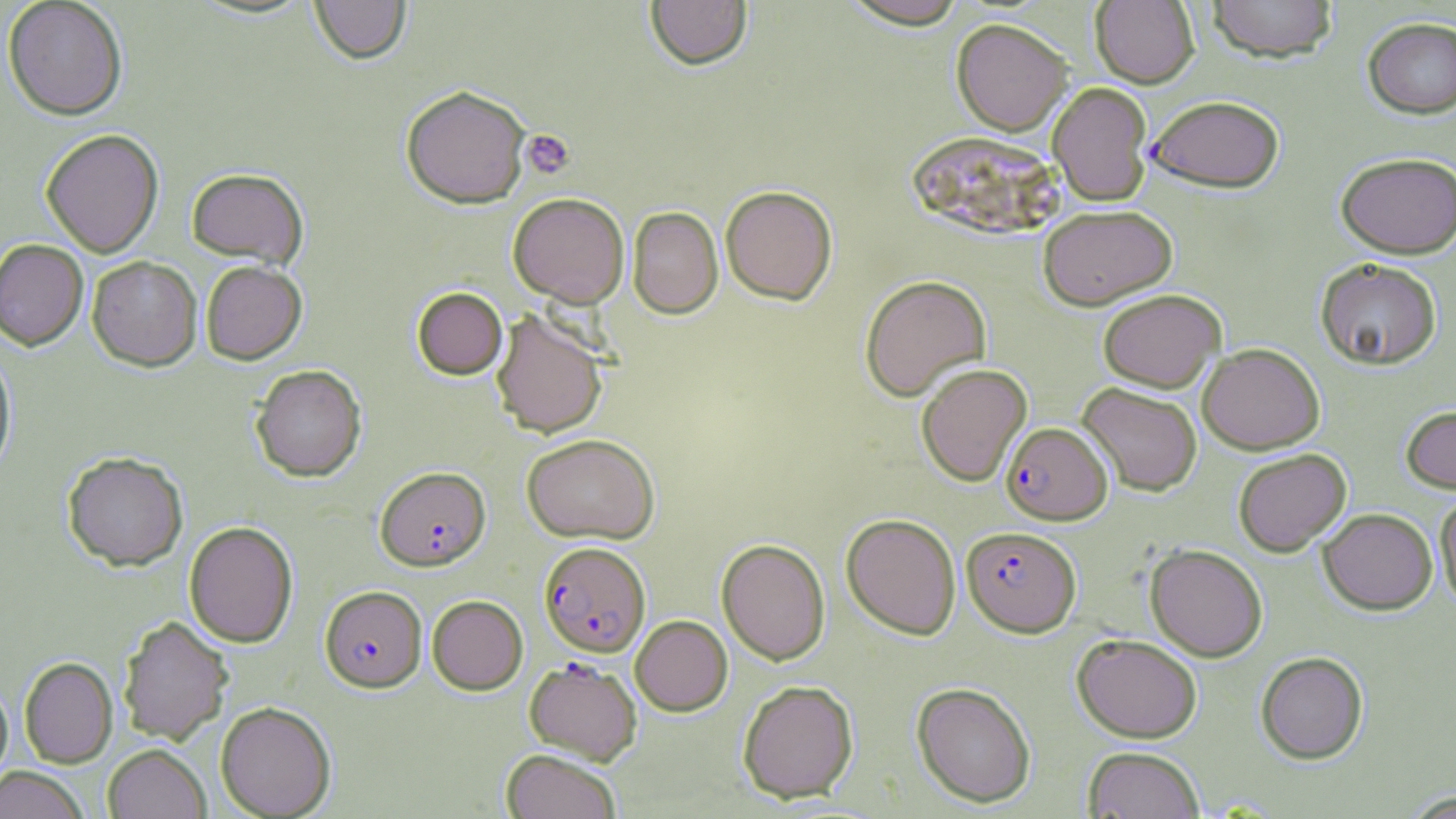

slide-level diagnosis = Plasmodium falciparum
image size = 1456×819 pixels
stain = May-Grünwald-Giemsa
uninfected red blood cell locations = approximate bounding boxes as named x1/y1/x2/y2 corners in pixels: (x1=309, y1=0, x2=411, y2=65), (x1=645, y1=0, x2=753, y2=70), (x1=1091, y1=0, x2=1199, y2=88), (x1=1205, y1=0, x2=1338, y2=62), (x1=2, y1=1, x2=128, y2=120), (x1=840, y1=1, x2=972, y2=29), (x1=1362, y1=16, x2=1456, y2=118), (x1=951, y1=18, x2=1072, y2=135), (x1=1047, y1=81, x2=1153, y2=205), (x1=400, y1=85, x2=531, y2=209), (x1=1147, y1=94, x2=1285, y2=192), (x1=40, y1=128, x2=164, y2=258), (x1=906, y1=131, x2=1063, y2=240), (x1=1335, y1=151, x2=1456, y2=258), (x1=186, y1=167, x2=309, y2=268), (x1=720, y1=185, x2=838, y2=305), (x1=508, y1=192, x2=630, y2=307), (x1=1038, y1=204, x2=1177, y2=310), (x1=627, y1=206, x2=723, y2=319), (x1=0, y1=239, x2=88, y2=350), (x1=87, y1=256, x2=202, y2=371), (x1=1315, y1=258, x2=1442, y2=369), (x1=200, y1=260, x2=307, y2=365), (x1=859, y1=274, x2=992, y2=401), (x1=412, y1=287, x2=507, y2=379), (x1=1097, y1=289, x2=1225, y2=392), (x1=491, y1=310, x2=608, y2=439), (x1=1198, y1=343, x2=1325, y2=454), (x1=0, y1=345, x2=17, y2=479), (x1=915, y1=363, x2=1032, y2=486), (x1=250, y1=364, x2=367, y2=482), (x1=1077, y1=382, x2=1203, y2=496), (x1=1400, y1=404, x2=1456, y2=494), (x1=521, y1=433, x2=660, y2=544), (x1=1233, y1=448, x2=1351, y2=556), (x1=61, y1=451, x2=188, y2=571), (x1=1435, y1=491, x2=1456, y2=610), (x1=1318, y1=508, x2=1437, y2=614), (x1=841, y1=513, x2=961, y2=639), (x1=184, y1=521, x2=298, y2=648), (x1=717, y1=538, x2=830, y2=665), (x1=1145, y1=544, x2=1267, y2=661), (x1=427, y1=595, x2=528, y2=695), (x1=118, y1=614, x2=234, y2=745), (x1=630, y1=615, x2=732, y2=716), (x1=1072, y1=633, x2=1203, y2=743), (x1=1255, y1=651, x2=1369, y2=764), (x1=19, y1=657, x2=117, y2=768), (x1=0, y1=679, x2=13, y2=788), (x1=737, y1=680, x2=859, y2=803), (x1=911, y1=682, x2=1036, y2=807), (x1=215, y1=701, x2=336, y2=818), (x1=103, y1=744, x2=211, y2=819), (x1=1082, y1=745, x2=1205, y2=818), (x1=500, y1=748, x2=622, y2=819), (x1=1, y1=767, x2=90, y2=819), (x1=1401, y1=790, x2=1455, y2=818)
preparation = thin blood smear
field of view = one of a larger specimen
Plasmodium falciparum-infected red blood cell locations = approximate bounding boxes as named x1/y1/x2/y2 corners in pixels: (x1=1001, y1=422, x2=1112, y2=525), (x1=375, y1=466, x2=491, y2=571), (x1=962, y1=526, x2=1081, y2=636), (x1=539, y1=541, x2=650, y2=657), (x1=320, y1=585, x2=427, y2=693), (x1=524, y1=658, x2=642, y2=765)
magnification = 1000x
platelet locations = approximate bounding boxes as named x1/y1/x2/y2 corners in pixels: (x1=520, y1=129, x2=575, y2=180)
modality = light microscopy